Outline each uninfected red blood cell.
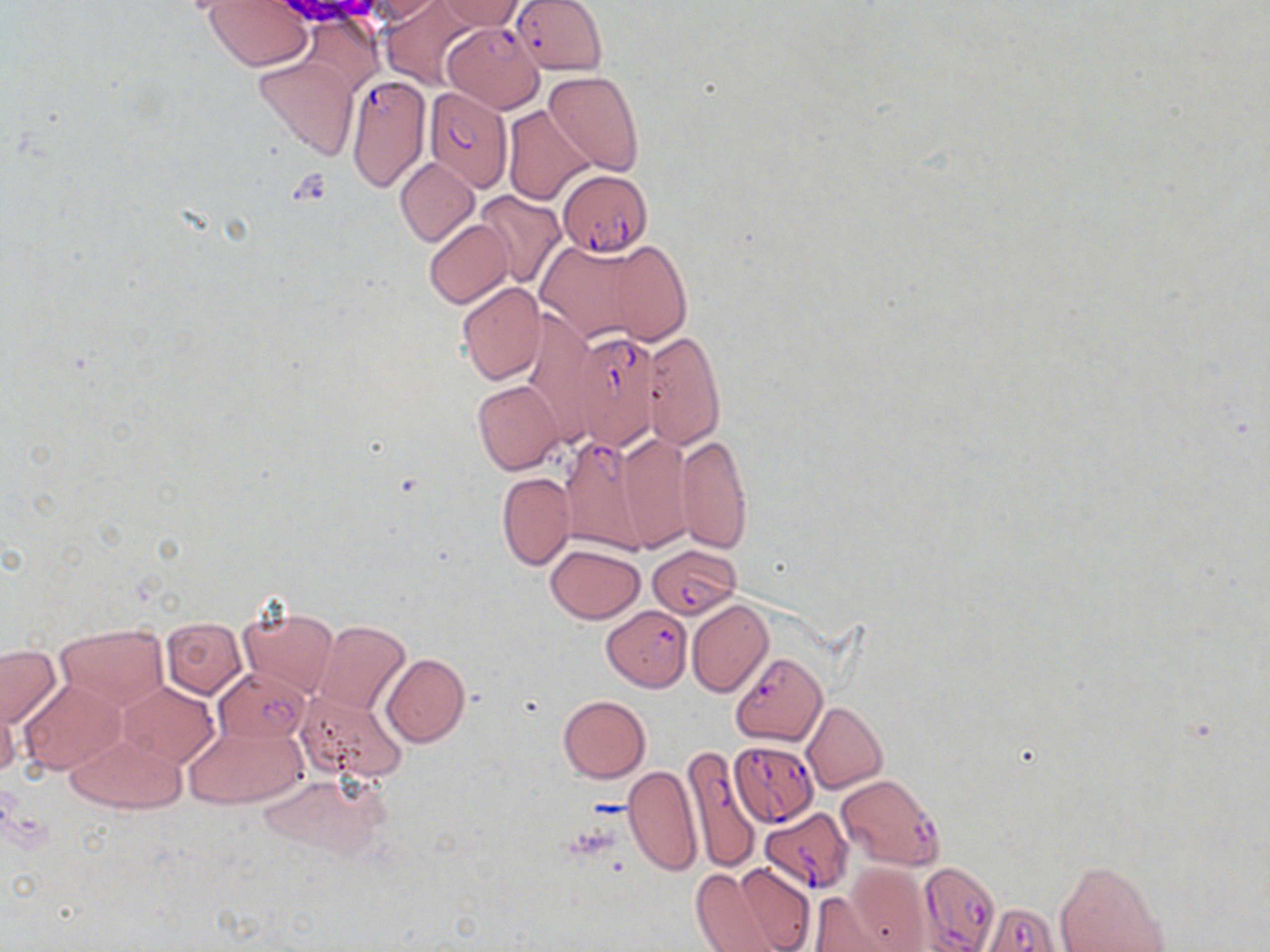

Approximate bounding boxes as [x1, y1, x2, y2] in pixels.
Uninfected red blood cells: [380, 0, 480, 88], [435, 0, 528, 32], [359, 1, 447, 25], [201, 3, 316, 70], [300, 17, 382, 96], [253, 54, 360, 160], [544, 70, 645, 175], [502, 104, 595, 205], [394, 158, 479, 246], [475, 191, 565, 288], [423, 218, 514, 309], [538, 235, 681, 347], [455, 281, 545, 385], [642, 331, 726, 448], [473, 380, 563, 475], [615, 433, 694, 550], [675, 434, 752, 554], [496, 472, 574, 570], [545, 544, 645, 622], [686, 600, 773, 697], [238, 606, 338, 698], [160, 617, 246, 698], [313, 621, 411, 717], [54, 624, 169, 708], [0, 644, 61, 728], [381, 654, 469, 746], [18, 680, 125, 773], [117, 680, 218, 767], [296, 689, 407, 782], [557, 695, 650, 783], [0, 698, 20, 782], [802, 701, 887, 794], [185, 722, 308, 809], [64, 730, 184, 815], [622, 766, 702, 876], [259, 774, 386, 860], [1054, 859, 1172, 952], [690, 863, 801, 952], [823, 868, 929, 951].

Summary:
  - Plasmodium falciparum-infected red blood cell locations: [511, 0, 607, 75], [443, 22, 545, 112], [344, 75, 431, 192], [423, 87, 511, 190], [559, 170, 652, 257], [565, 327, 662, 450], [560, 435, 652, 557], [648, 545, 740, 619], [602, 605, 691, 691], [730, 652, 827, 746], [215, 667, 309, 743], [729, 741, 819, 826], [681, 749, 762, 874], [836, 774, 946, 872], [759, 806, 853, 895], [919, 865, 1001, 952], [982, 903, 1063, 952]
  - Slide-level diagnosis: Plasmodium falciparum
  - Field of view: single
  - Magnification: 1000x
  - Stain: May-Grünwald-Giemsa
  - Modality: light microscopy
  - Image size: 1270×952 pixels
  - Preparation: thin blood film